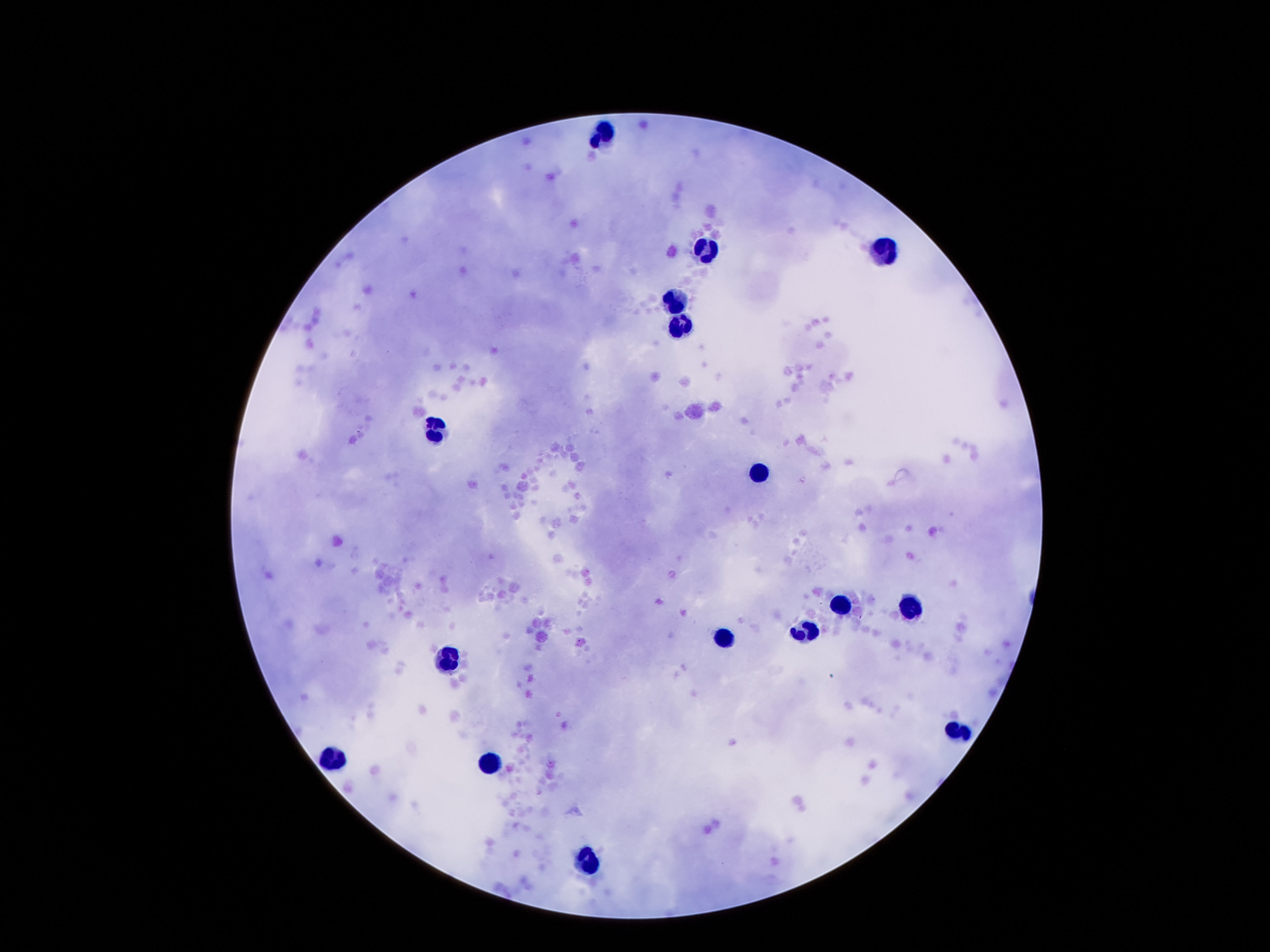
Approximate object centers, in pixels from the top-left corner. Leukocyte locations: (x=606, y=134), (x=705, y=246), (x=892, y=251), (x=673, y=295), (x=678, y=326), (x=433, y=427), (x=760, y=472), (x=839, y=597), (x=911, y=609), (x=808, y=628), (x=726, y=635), (x=455, y=659), (x=959, y=729), (x=335, y=758), (x=493, y=765), (x=587, y=854). One field from this slide. Image is 1270×952 pixels. 100x magnification. Thick blood film. Patient malaria status: not infected. Smartphone photograph taken through the microscope eyepiece. Giemsa stain.